Locate every leukocyte (white blood cell).
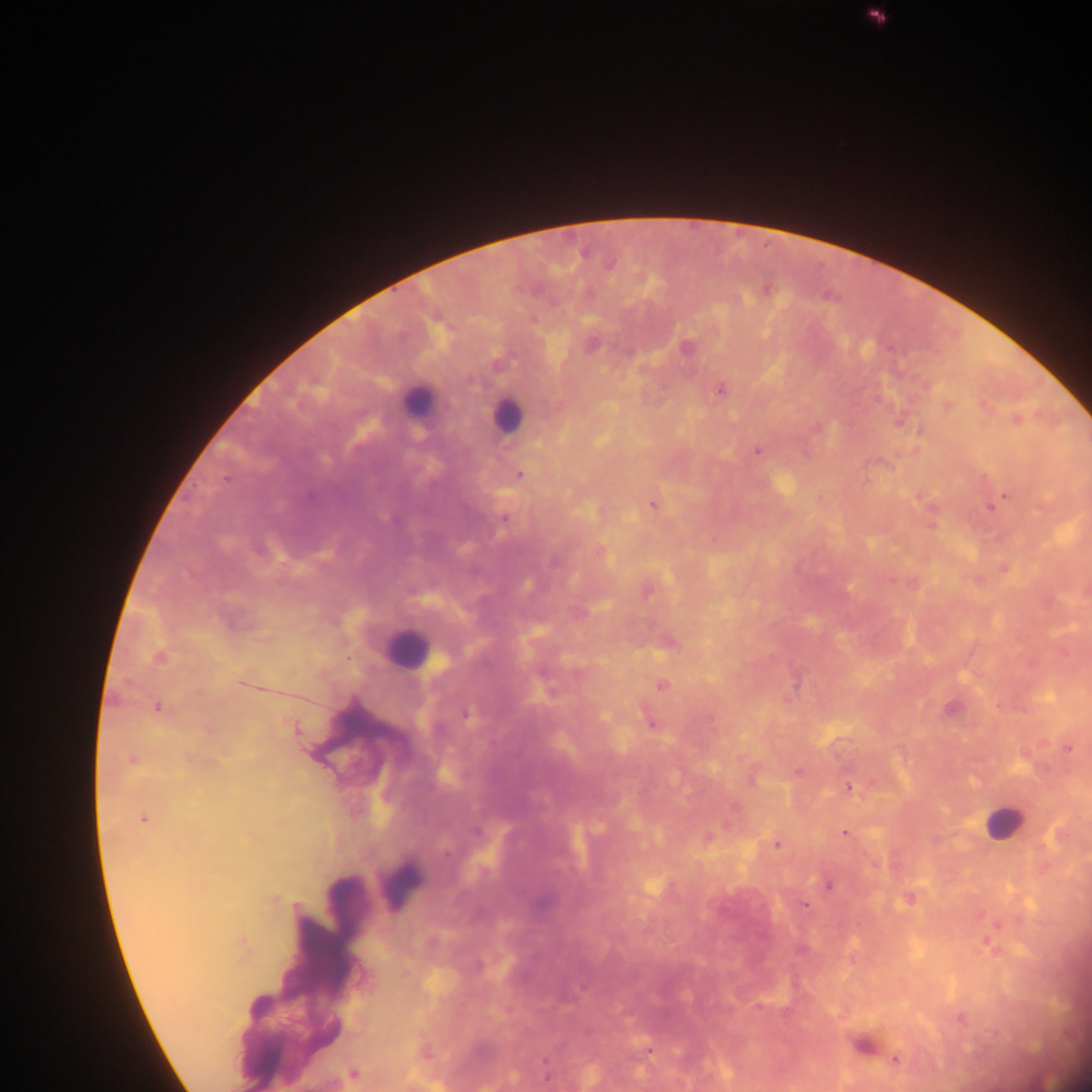
Approximate centers as [x, y] in pixels.
Leukocytes: [415, 400], [506, 415], [406, 648], [1002, 823], [400, 883].

Summary:
  - Plasmodium parasite locations: [583, 254], [610, 265], [591, 346], [686, 347], [720, 390], [948, 405], [1016, 420], [757, 451], [519, 475], [1002, 499], [653, 505], [993, 506], [503, 519], [259, 549], [554, 562], [892, 580], [158, 658], [241, 683], [661, 686], [157, 707], [465, 714], [651, 724], [295, 728], [1069, 748], [132, 761], [798, 772], [849, 787], [143, 819], [475, 832], [845, 833], [708, 837], [777, 845], [828, 885], [805, 906], [646, 1051], [896, 1059], [353, 1074]
  - Capture: mobile-phone photograph through a microscope
  - Preparation: thick blood film
  - Field of view: single
  - Image size: 1092×1092 pixels
  - Country: Ghana